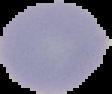

Summary:
  - Result: negative for Plasmodium parasites
  - Image size: 112×94 pixels
  - Preparation: thin blood smear
  - Image type: cell region segmented out of the field of view; surrounding area masked to black